Point out each Plasmodium parasite.
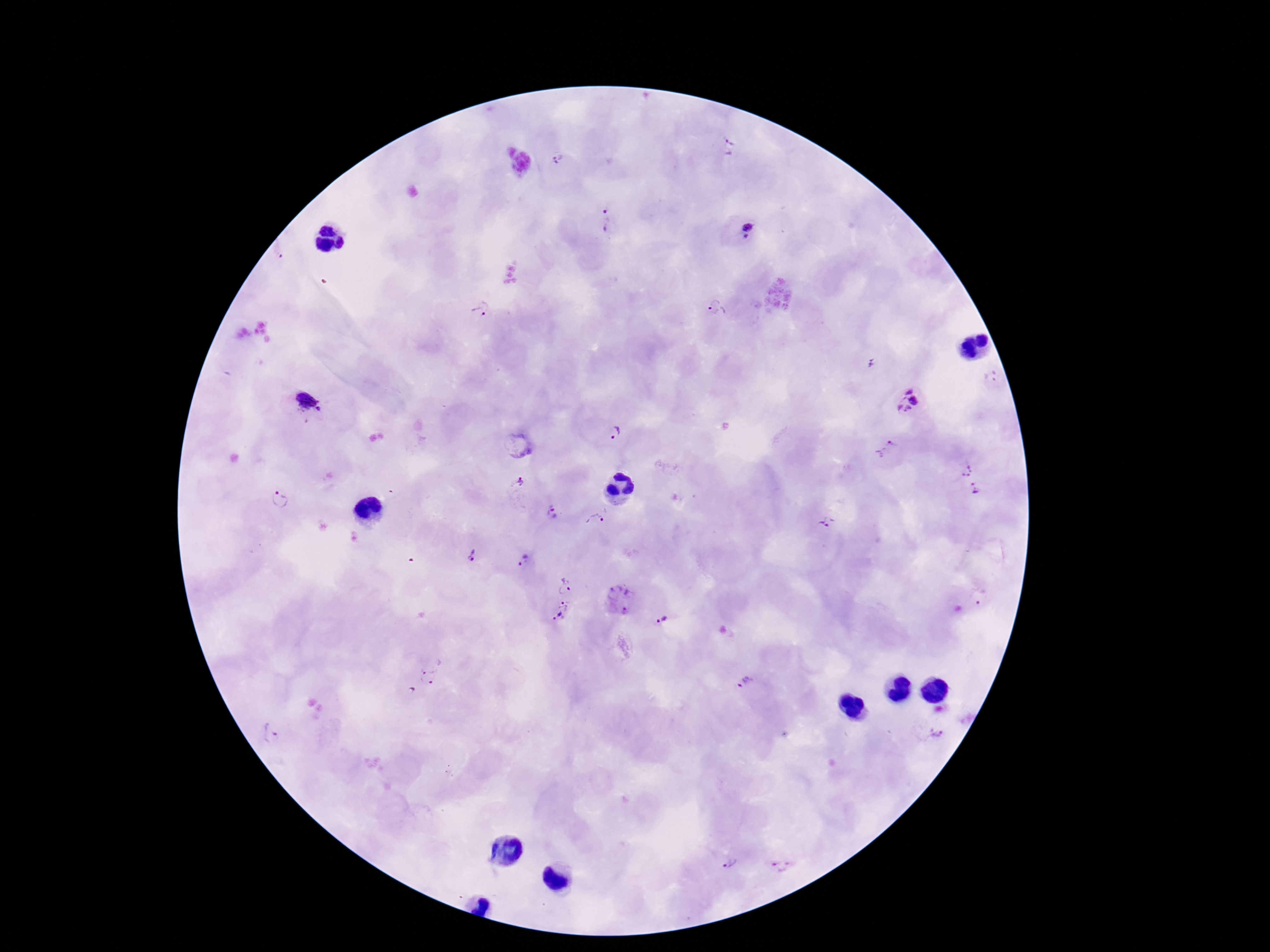
Approximate centers as [x, y] in pixels.
Plasmodium parasites: [727, 146], [558, 160], [605, 218], [748, 231], [480, 308], [717, 308], [991, 378], [909, 400], [304, 405], [615, 432], [886, 450], [964, 467], [520, 487], [975, 489], [279, 499], [552, 513], [596, 520], [826, 523], [472, 556], [525, 561], [565, 585], [982, 595], [620, 599], [561, 612], [663, 619], [429, 677], [746, 681], [936, 731], [270, 733], [728, 861], [781, 864].

Summary:
  - Stain: Giemsa
  - Magnification: 100x
  - Preparation: thick peripheral-blood smear
  - Patient malaria status: infected
  - Field of view: one from this slide
  - Capture: smartphone camera through the microscope eyepiece
  - Image size: 1270×952 pixels